Describe the morphology of the red blood cells.
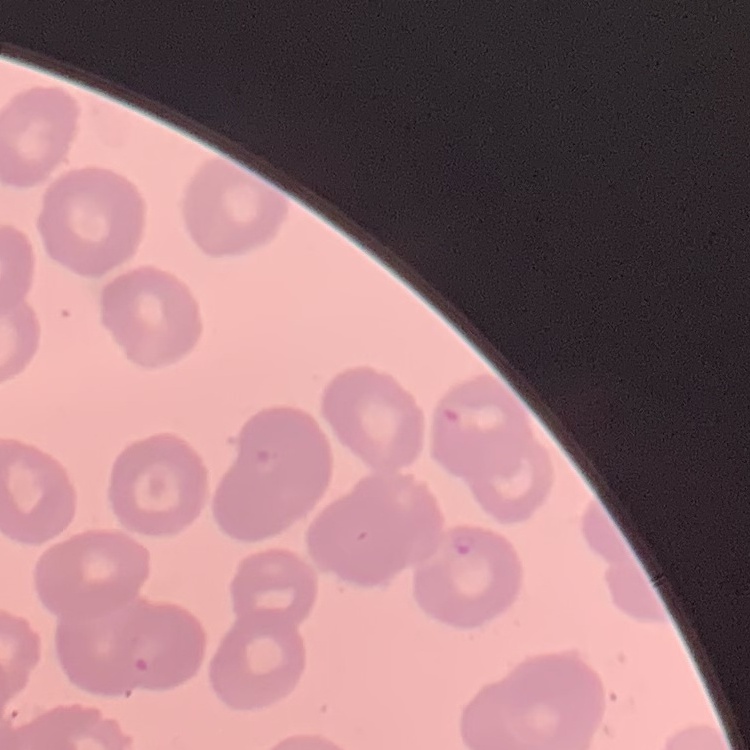
They show no rouleaux formation.

Thin blood film. Field's or Giemsa stain. One tile cut from a larger photomicrograph.